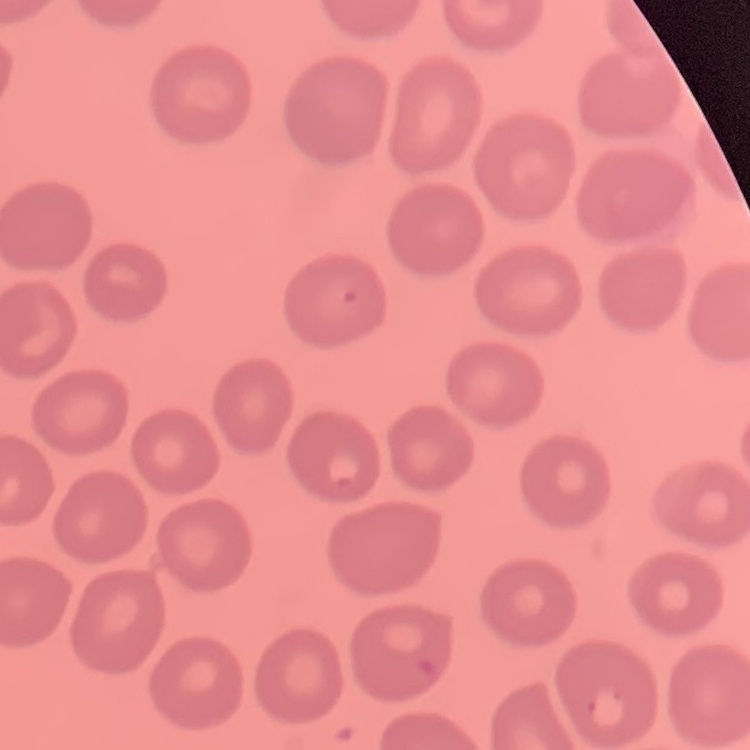

Summary:
  - Erythrocyte morphology: no rouleaux formation
  - Image type: square crop of a larger photomicrograph
  - Stain: Field's or Giemsa
  - Preparation: thin blood smear